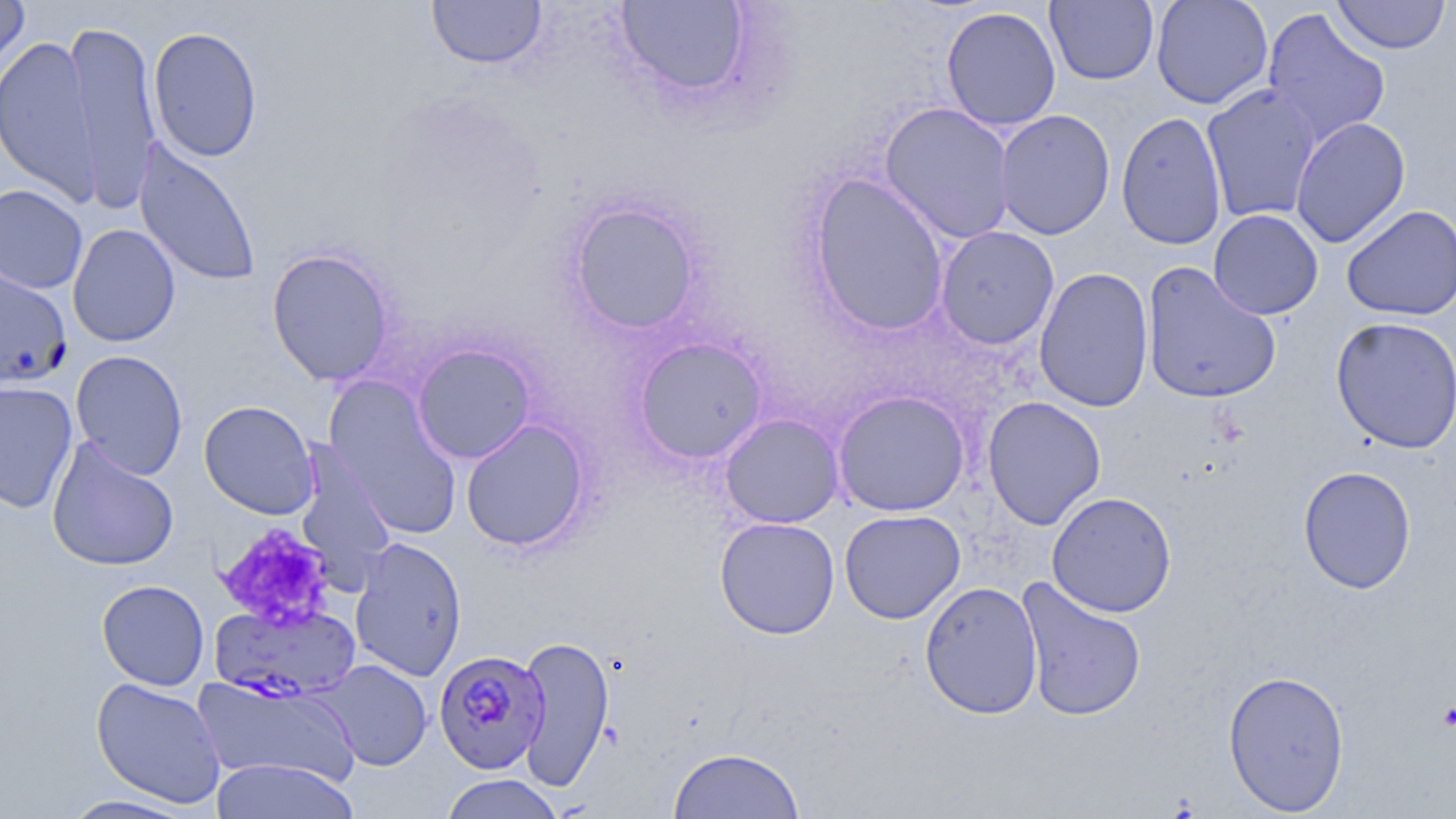

Summary:
  - Coordinate format: approximate bounding boxes as (x1, y1, x2, y2) in pixels
  - Uninfected red blood cell locations: (0, 0, 30, 75), (426, 0, 547, 70), (1151, 0, 1274, 109), (1331, 0, 1450, 55), (615, 1, 752, 100), (1045, 1, 1159, 85), (940, 6, 1061, 131), (1261, 7, 1391, 150), (65, 18, 162, 210), (148, 26, 263, 162), (0, 35, 102, 205), (1200, 83, 1322, 223), (879, 103, 1016, 244), (994, 109, 1115, 239), (1116, 110, 1227, 250), (1290, 116, 1411, 248), (133, 140, 261, 287), (808, 174, 949, 336), (0, 184, 89, 294), (567, 200, 704, 336), (1341, 204, 1456, 321), (1208, 209, 1323, 320), (67, 223, 180, 347), (935, 226, 1059, 350), (266, 248, 396, 386), (1142, 261, 1281, 405), (0, 266, 73, 388), (1034, 266, 1154, 413), (1330, 315, 1456, 455), (634, 337, 768, 464), (411, 344, 537, 464), (70, 350, 189, 480), (325, 378, 462, 540), (0, 381, 78, 514), (833, 391, 970, 516), (982, 396, 1106, 530), (199, 400, 320, 520), (720, 413, 844, 528), (461, 419, 589, 552), (47, 438, 180, 572), (293, 440, 397, 591), (1297, 466, 1417, 594), (1047, 491, 1177, 617), (839, 509, 966, 624), (714, 516, 840, 639), (349, 537, 467, 681), (1016, 576, 1147, 723), (96, 579, 210, 691), (920, 581, 1043, 719), (516, 633, 614, 793), (313, 659, 433, 771), (1223, 669, 1350, 815), (192, 673, 360, 787), (91, 677, 228, 808), (668, 747, 805, 819), (210, 758, 360, 819), (439, 774, 563, 819), (56, 794, 202, 818)
  - Platelet locations: (217, 522, 336, 630), (1437, 700, 1456, 732)
  - Plasmodium falciparum-infected red blood cell locations: (209, 600, 363, 703), (434, 649, 549, 774)
  - Slide-level diagnosis: Plasmodium falciparum
  - Field of view: single
  - Modality: optical microscopy
  - Magnification: 1000x
  - Image size: 1456×819 pixels
  - Stain: May-Grünwald-Giemsa
  - Preparation: thin blood smear